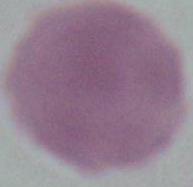

Summary:
  - Identification: red blood cell
  - Magnification: 1000x
  - Modality: photomicrograph